Report the malaria status.
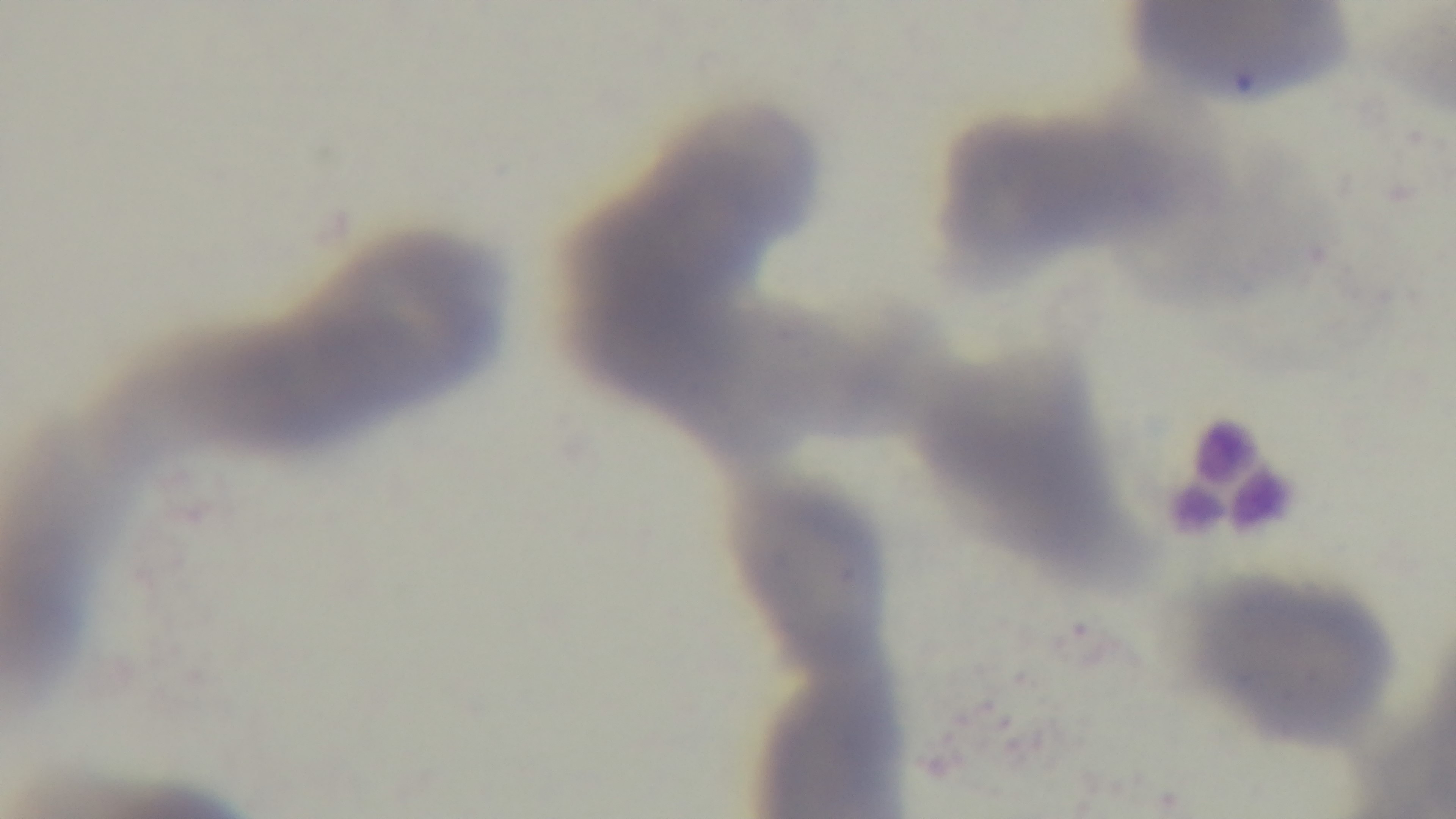

Uninfected.

field of view = single
stain = Giemsa
modality = light microscopy
objective = 100x oil immersion
capture = mounted 4K digital camera
preparation = thin smear